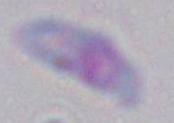
modality: photomicrograph
identification: Toxoplasma gondii
magnification: 1000x